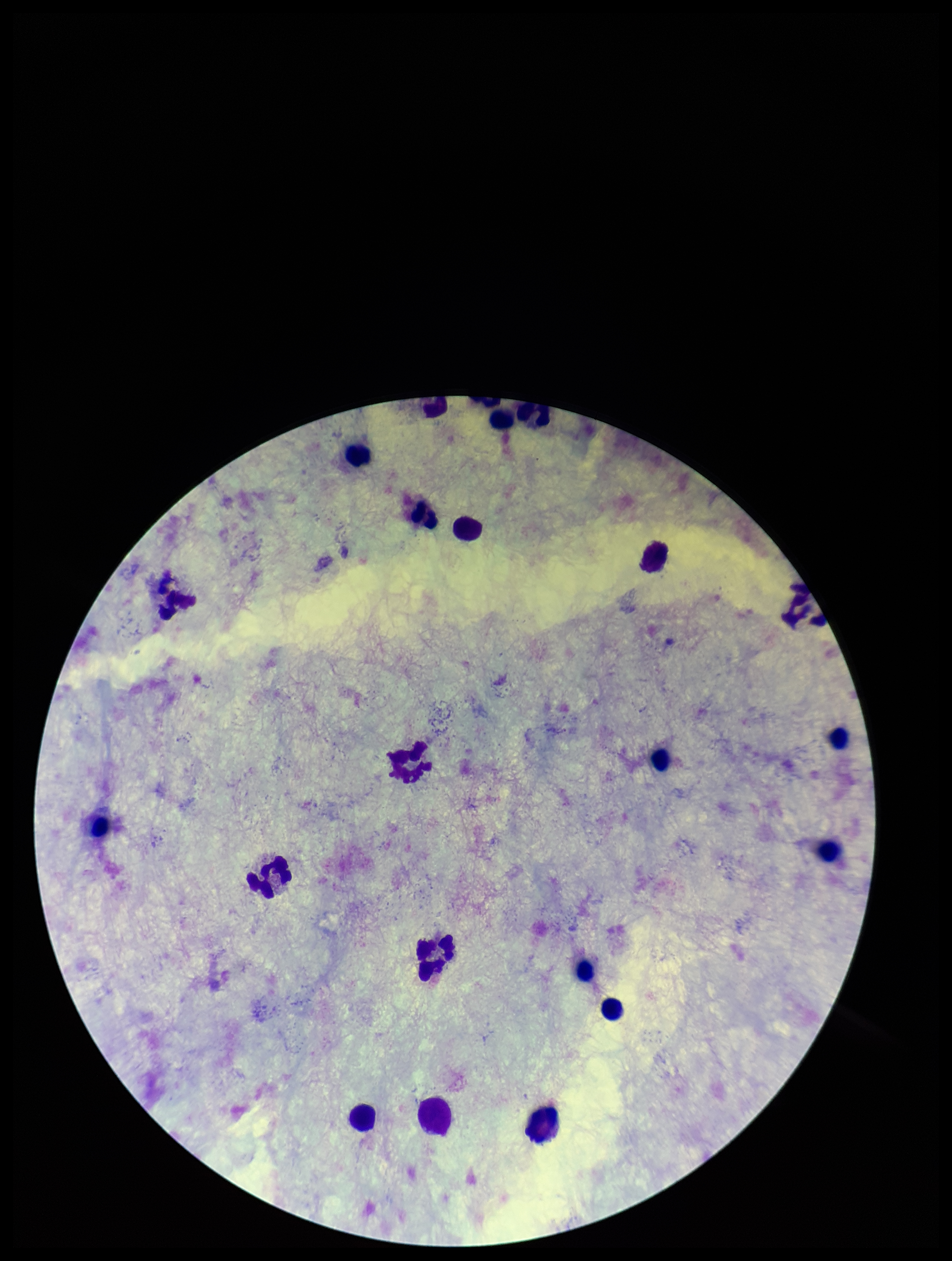 One field from this slide. Patient malaria status: negative. Preparation: thick smear. Image is 952×1261 pixels. Leukocyte count: 20. Photographed through the microscope eyepiece with a smartphone camera. Giemsa stain. Plasmodium parasites: none detected. Parasite count: 0.